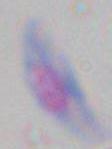
Summary:
  - Magnification: 1000x
  - Identification: Toxoplasma gondii
  - Modality: micrograph